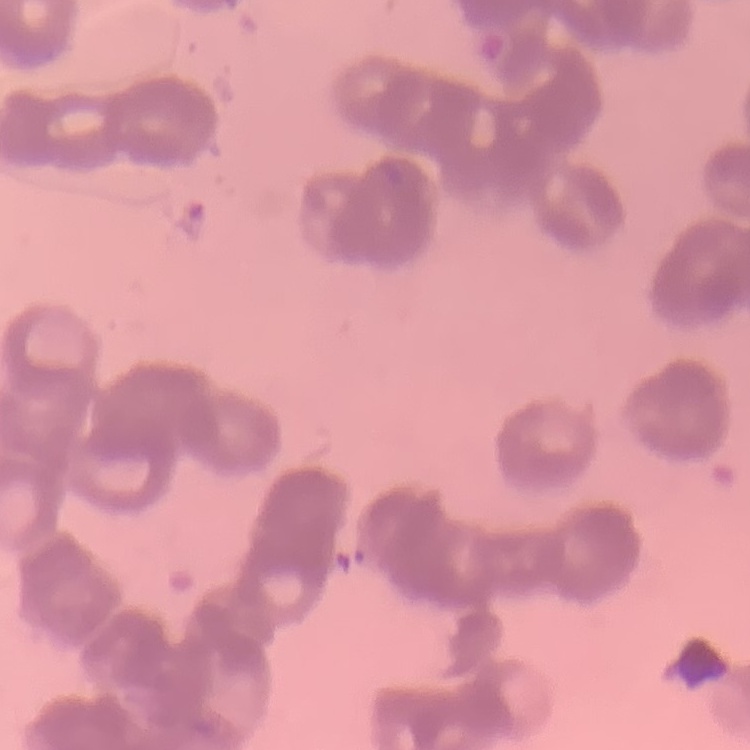 The erythrocytes show rouleaux formation. One tile cut from a larger photomicrograph. Stained with either Field's or Giemsa. Thin blood film.